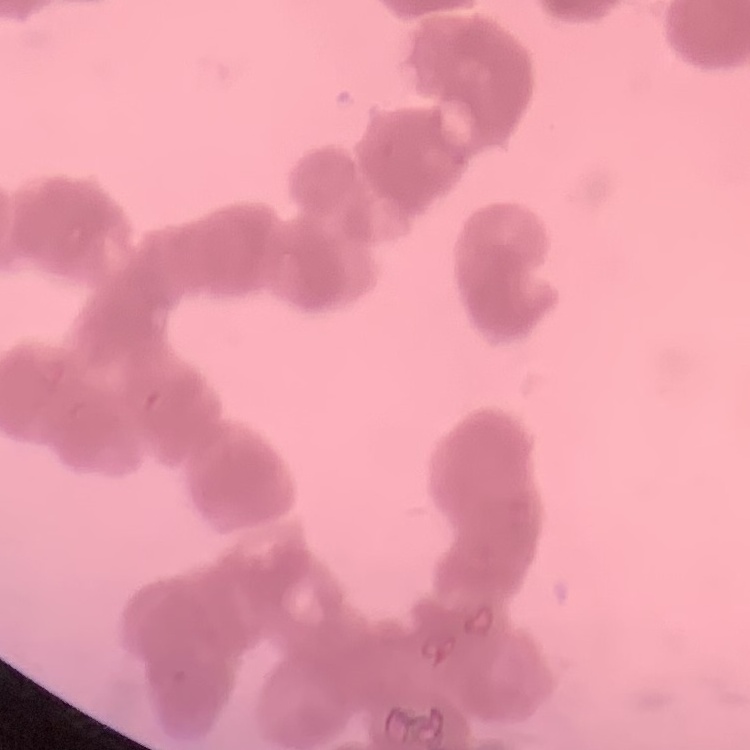 The erythrocytes show rouleaux formation. Square crop of a larger photomicrograph. Thin blood smear. Stained with either Field's or Giemsa.